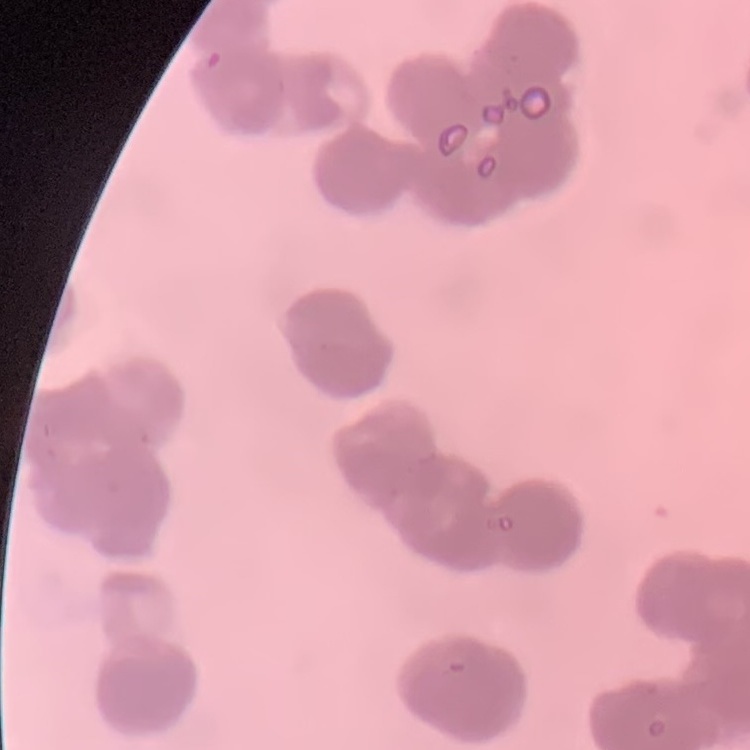

The red blood cells exhibit rouleaux formation. Stained with either Field's or Giemsa. Square crop of a larger photomicrograph. Thin blood smear.